Describe the morphology of the erythrocytes.
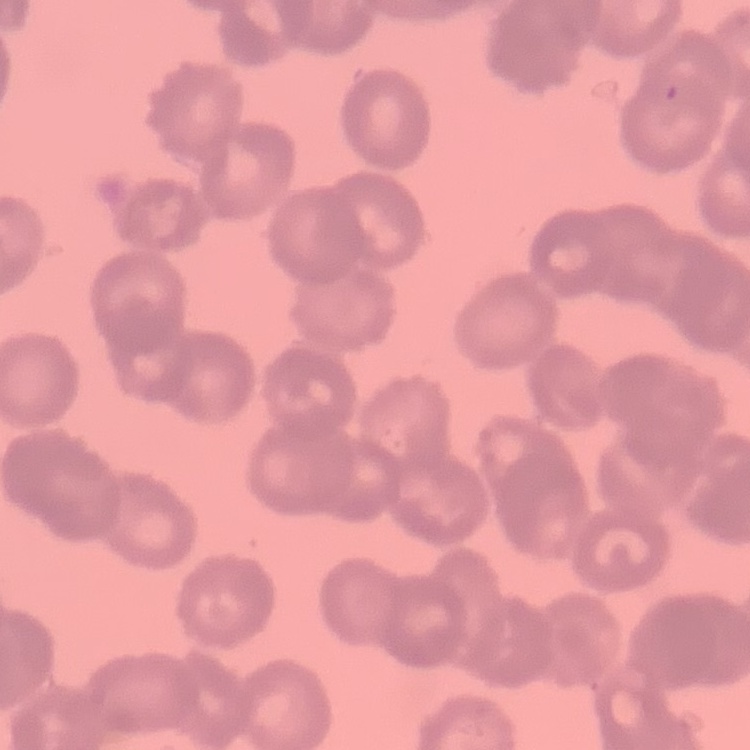

Rouleaux formation.

Stained with either Field's or Giemsa. Thin blood film. Square crop of a larger photomicrograph.